Describe the morphology of the red blood cells.
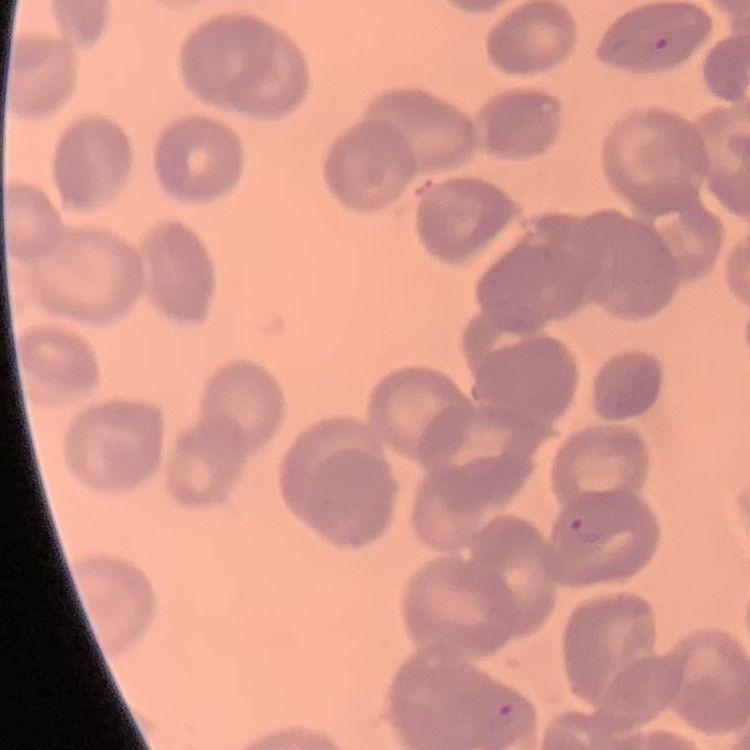
No rouleaux formation.

image type = one tile cut from a larger photomicrograph
preparation = thin peripheral smear
stain = Field's or Giemsa